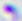

Captured at 400x magnification. Photomicrograph. Toxoplasma gondii is seen.